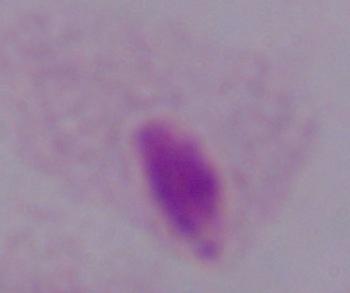
Micrograph. A trichomonad is seen. Captured at 1000x magnification.